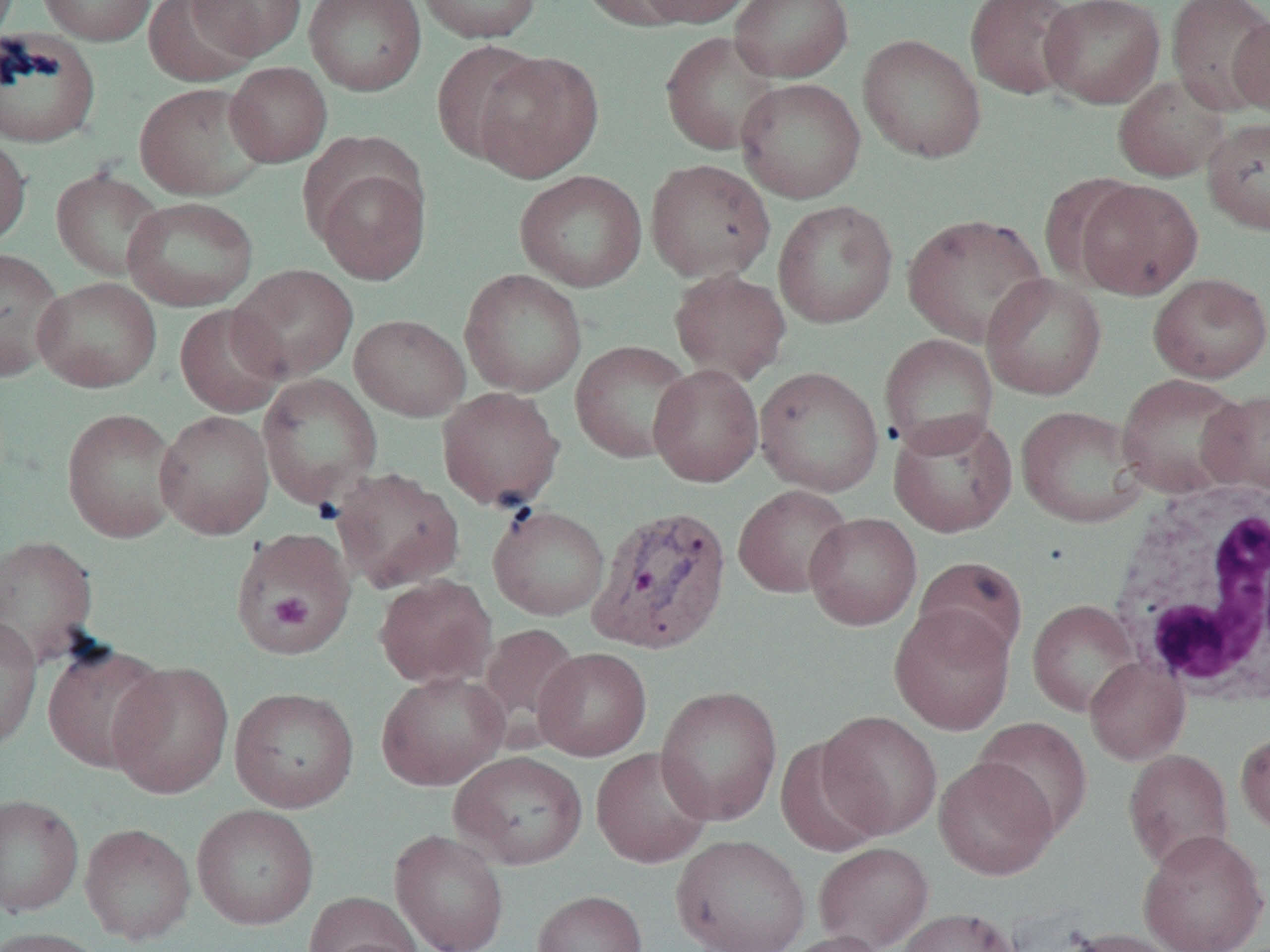

slide-level diagnosis = Plasmodium vivax
field of view = one of a larger specimen
uninfected red blood cell locations = approximate bounding boxes as named x1/y1/x2/y2 corners in pixels: (x1=37, y1=0, x2=156, y2=46), (x1=186, y1=0, x2=307, y2=61), (x1=304, y1=0, x2=426, y2=96), (x1=414, y1=0, x2=543, y2=43), (x1=576, y1=0, x2=698, y2=30), (x1=634, y1=0, x2=756, y2=27), (x1=729, y1=0, x2=854, y2=82), (x1=965, y1=0, x2=1082, y2=100), (x1=1039, y1=0, x2=1165, y2=108), (x1=1166, y1=0, x2=1270, y2=116), (x1=146, y1=1, x2=258, y2=87), (x1=1228, y1=12, x2=1270, y2=117), (x1=0, y1=27, x2=102, y2=149), (x1=660, y1=31, x2=782, y2=155), (x1=858, y1=34, x2=986, y2=163), (x1=431, y1=40, x2=547, y2=164), (x1=471, y1=50, x2=604, y2=182), (x1=225, y1=62, x2=332, y2=167), (x1=1112, y1=74, x2=1230, y2=182), (x1=735, y1=77, x2=866, y2=204), (x1=134, y1=82, x2=270, y2=200), (x1=1202, y1=117, x2=1270, y2=236), (x1=0, y1=132, x2=31, y2=249), (x1=645, y1=158, x2=775, y2=284), (x1=314, y1=163, x2=431, y2=284), (x1=50, y1=168, x2=166, y2=281), (x1=514, y1=170, x2=647, y2=292), (x1=1071, y1=179, x2=1203, y2=300), (x1=123, y1=196, x2=259, y2=311), (x1=773, y1=199, x2=898, y2=329), (x1=902, y1=212, x2=1048, y2=347), (x1=0, y1=248, x2=66, y2=380), (x1=229, y1=264, x2=359, y2=382), (x1=459, y1=268, x2=587, y2=397), (x1=669, y1=269, x2=791, y2=385), (x1=981, y1=273, x2=1107, y2=400), (x1=1148, y1=273, x2=1270, y2=383), (x1=32, y1=276, x2=161, y2=393), (x1=174, y1=304, x2=289, y2=418), (x1=350, y1=314, x2=471, y2=421), (x1=879, y1=333, x2=998, y2=457), (x1=570, y1=340, x2=694, y2=463), (x1=648, y1=363, x2=763, y2=487), (x1=754, y1=366, x2=884, y2=497), (x1=1115, y1=372, x2=1251, y2=498), (x1=257, y1=374, x2=383, y2=509), (x1=437, y1=386, x2=565, y2=511), (x1=1199, y1=389, x2=1270, y2=496), (x1=1016, y1=405, x2=1149, y2=528), (x1=62, y1=408, x2=181, y2=543), (x1=155, y1=409, x2=275, y2=540), (x1=888, y1=411, x2=1017, y2=538), (x1=331, y1=467, x2=465, y2=594), (x1=732, y1=485, x2=853, y2=598), (x1=487, y1=505, x2=610, y2=620), (x1=804, y1=512, x2=923, y2=630), (x1=229, y1=527, x2=355, y2=655), (x1=0, y1=534, x2=99, y2=667), (x1=914, y1=556, x2=1028, y2=663), (x1=373, y1=574, x2=496, y2=688), (x1=1027, y1=600, x2=1141, y2=717), (x1=888, y1=604, x2=1016, y2=735), (x1=0, y1=615, x2=42, y2=751), (x1=477, y1=622, x2=582, y2=744), (x1=42, y1=640, x2=170, y2=773), (x1=533, y1=647, x2=652, y2=761), (x1=1085, y1=656, x2=1190, y2=765), (x1=106, y1=661, x2=234, y2=799), (x1=375, y1=670, x2=510, y2=791), (x1=655, y1=685, x2=783, y2=826), (x1=229, y1=686, x2=359, y2=812), (x1=817, y1=711, x2=943, y2=839), (x1=973, y1=717, x2=1092, y2=838), (x1=1235, y1=730, x2=1270, y2=837), (x1=774, y1=737, x2=886, y2=857), (x1=590, y1=747, x2=714, y2=868), (x1=1123, y1=748, x2=1234, y2=872), (x1=450, y1=751, x2=588, y2=870), (x1=934, y1=757, x2=1059, y2=880), (x1=0, y1=793, x2=84, y2=917), (x1=192, y1=804, x2=320, y2=929), (x1=80, y1=823, x2=196, y2=944), (x1=389, y1=829, x2=510, y2=952), (x1=1137, y1=829, x2=1269, y2=952), (x1=672, y1=834, x2=810, y2=952), (x1=813, y1=841, x2=934, y2=951), (x1=532, y1=889, x2=647, y2=952), (x1=303, y1=891, x2=422, y2=952), (x1=895, y1=907, x2=1020, y2=952), (x1=0, y1=927, x2=109, y2=952), (x1=1058, y1=927, x2=1187, y2=952), (x1=775, y1=930, x2=890, y2=952), (x1=314, y1=938, x2=426, y2=952)
image size = 1270×952 pixels
preparation = thin blood smear
Plasmodium vivax-infected red blood cell locations = approximate bounding boxes as named x1/y1/x2/y2 corners in pixels: (x1=587, y1=503, x2=732, y2=654)
white blood cell locations = approximate bounding boxes as named x1/y1/x2/y2 corners in pixels: (x1=1107, y1=480, x2=1270, y2=705)
platelet locations = approximate bounding boxes as named x1/y1/x2/y2 corners in pixels: (x1=270, y1=592, x2=313, y2=630)
magnification = 1000x
modality = light microscopy